Point out each Plasmodium parasite.
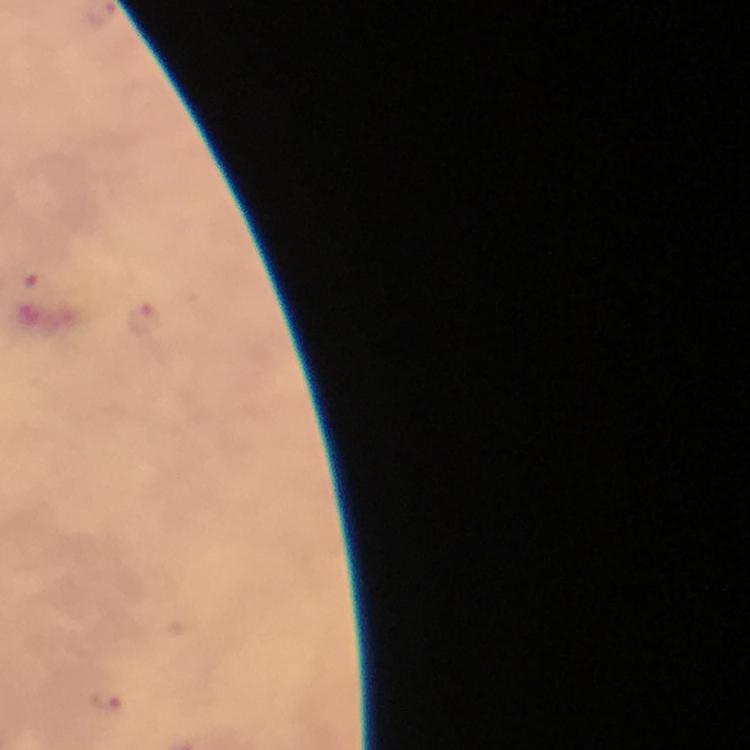

Approximate centers as (x, y) in pixels.
Plasmodium parasites: (32, 276), (143, 321), (109, 704).

context = from a diagnostic examination for malaria
capture = smartphone mounted on the microscope
magnification = 100x
image size = 750×750 pixels
stain = Giemsa
cropped from = a single field of view
immersion oil = used
preparation = thick smear